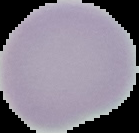 Result: no Plasmodium parasites detected. The area outside the segmented cell region is set to black. Image is 139×133 pixels. From a thin blood film.